Classify this cell by malaria status.
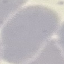
It is uninfected.

Automatically extracted cell patch, resized to 64 × 64 pixels. Thin blood film. Giemsa stain. Acquired by smartphone through the microscope eyepiece.